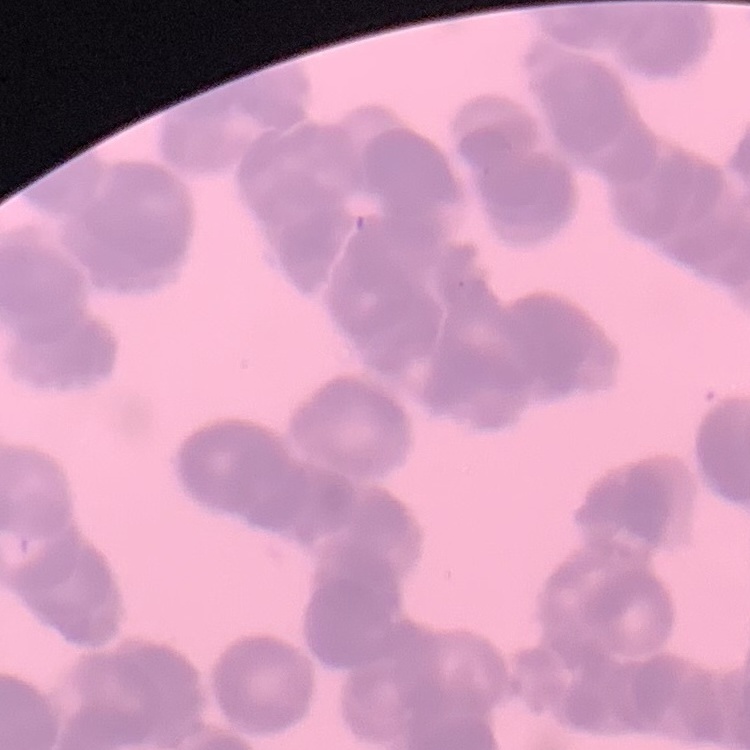

Summary:
  - Red blood cell morphology: rouleaux formation
  - Stain: Field's or Giemsa
  - Image type: square crop of a larger photomicrograph
  - Preparation: thin blood smear